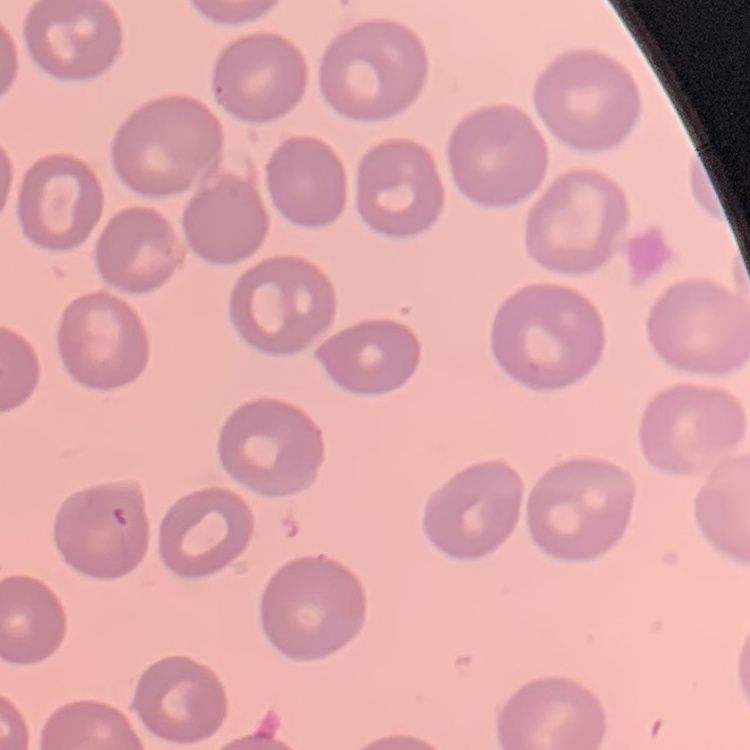

erythrocyte_morphology: no rouleaux formation
image_type: one tile cut from a larger photomicrograph
stain: Field's or Giemsa
preparation: thin blood film